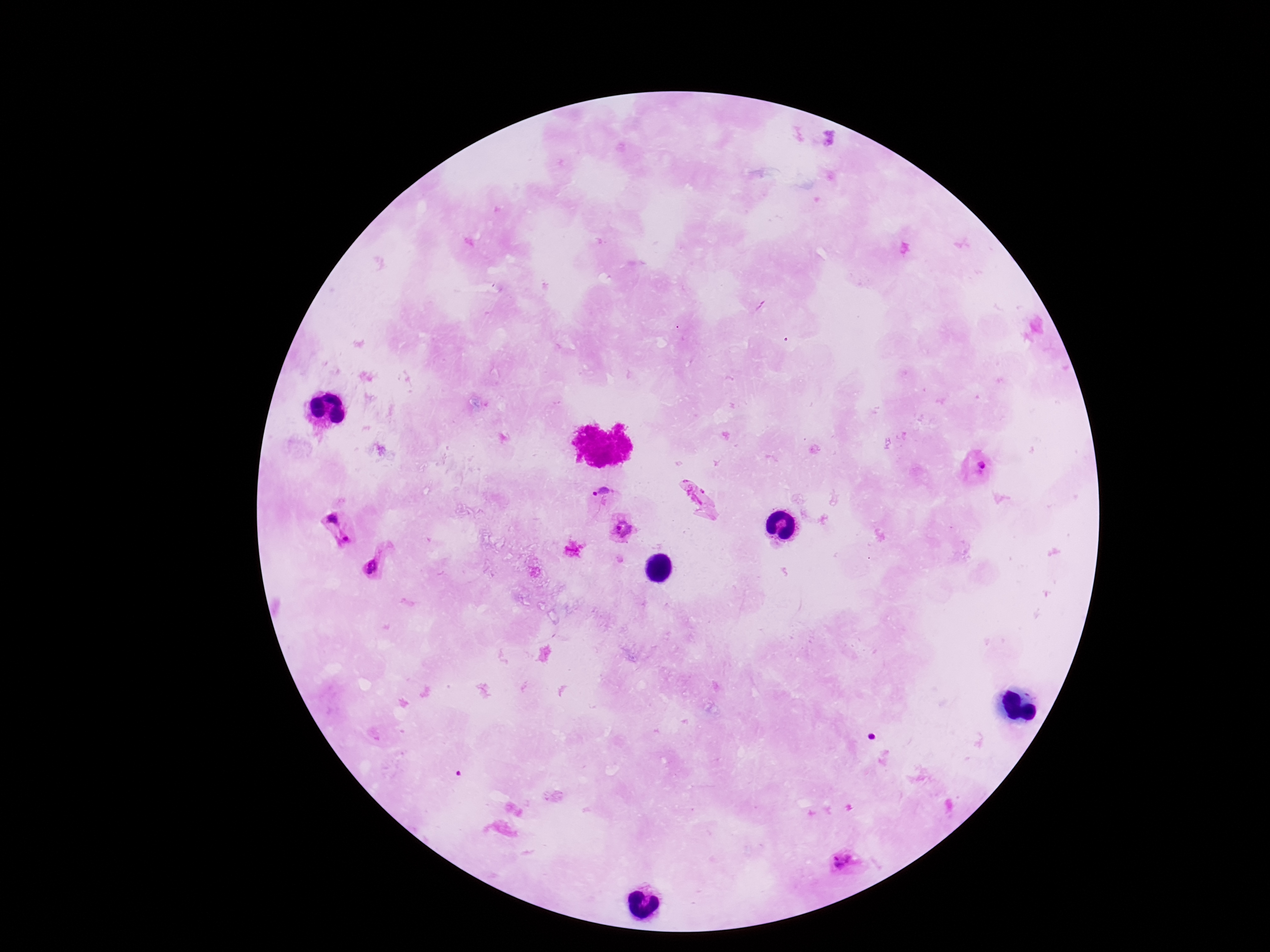

Approximate centers as [x, y] in pixels.
Summary:
  - Plasmodium parasite locations: [979, 471], [697, 498], [603, 499], [342, 530], [623, 533], [375, 564], [847, 863]
  - Image size: 1270×952 pixels
  - Magnification: 100x
  - Preparation: thick blood film
  - Capture: smartphone camera through the microscope eyepiece
  - Stain: Giemsa
  - Patient malaria status: infected
  - Field of view: single